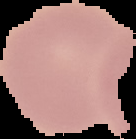

malaria status = uninfected
image size = 136×139 pixels
image type = segmented cell region on a black background
preparation = thin blood film